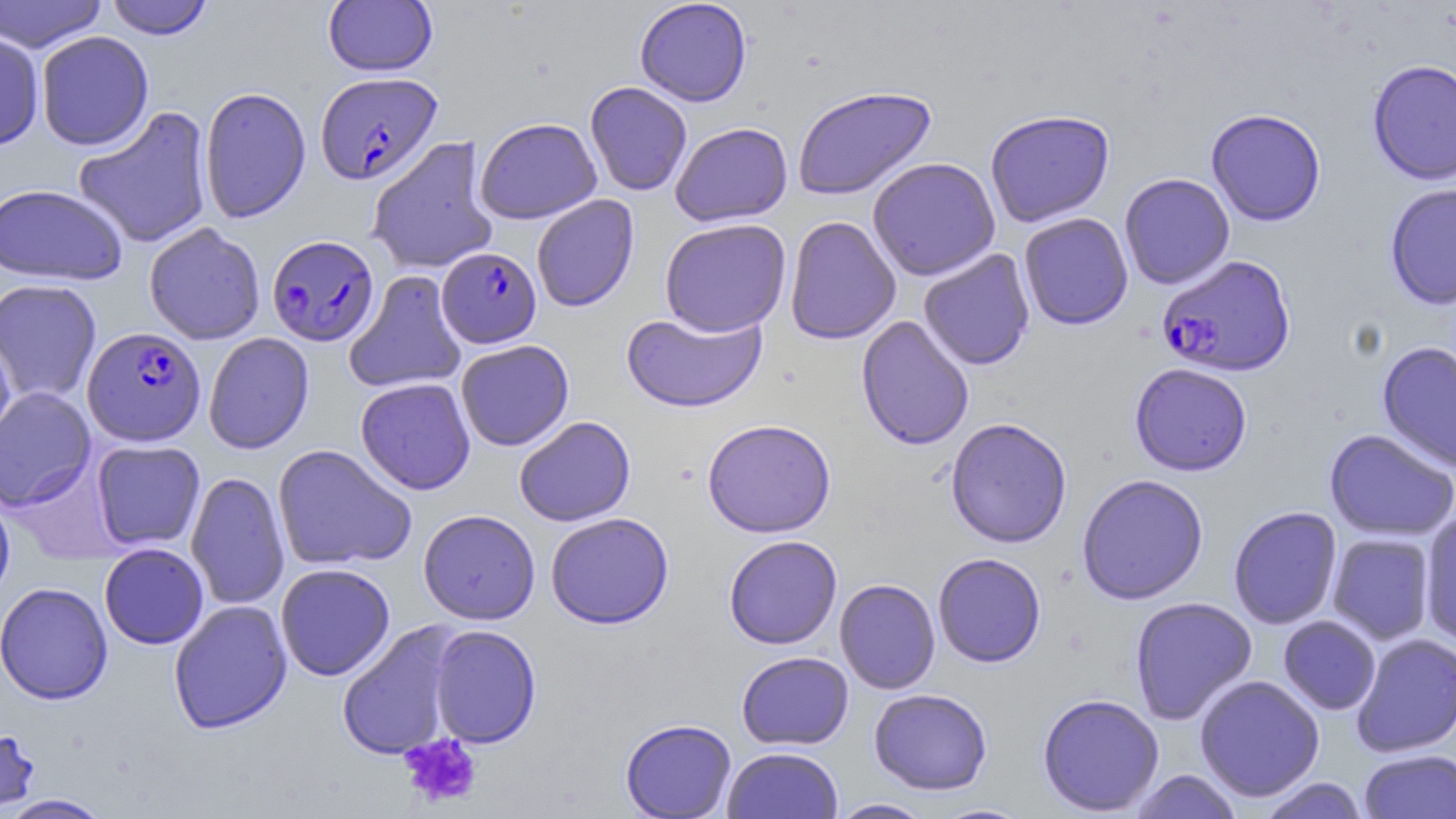

Approximate bounding boxes as (x1, y1, x2, y2) in pixels. Uninfected red blood cell locations: (0, 0, 109, 53), (104, 0, 215, 40), (634, 0, 752, 107), (323, 1, 438, 76), (0, 29, 45, 152), (35, 31, 154, 150), (1367, 59, 1456, 186), (585, 81, 693, 196), (792, 85, 937, 200), (199, 86, 311, 224), (73, 106, 214, 249), (1206, 108, 1326, 227), (985, 110, 1115, 227), (474, 117, 602, 224), (670, 121, 793, 227), (367, 136, 499, 274), (867, 157, 1001, 281), (1119, 173, 1235, 289), (0, 183, 128, 285), (1384, 184, 1456, 310), (531, 195, 640, 312), (1019, 212, 1133, 331), (784, 216, 901, 345), (659, 218, 792, 336), (144, 223, 266, 345), (918, 249, 1035, 370), (344, 270, 468, 394), (0, 279, 102, 405), (621, 310, 767, 413), (856, 316, 974, 451), (0, 331, 17, 461), (203, 333, 314, 455), (455, 339, 574, 451), (1376, 341, 1456, 474), (1129, 363, 1252, 476), (355, 377, 476, 495), (0, 387, 96, 512), (514, 416, 636, 527), (945, 417, 1072, 548), (702, 419, 836, 538), (1323, 429, 1456, 541), (91, 440, 206, 550), (273, 444, 416, 572), (186, 472, 290, 610), (1076, 474, 1209, 605), (0, 486, 16, 610), (1228, 505, 1342, 630), (418, 509, 540, 624), (1419, 510, 1456, 648), (545, 512, 674, 629), (1327, 533, 1436, 644), (723, 535, 843, 649), (99, 544, 209, 650), (932, 553, 1046, 668), (275, 563, 395, 681), (835, 578, 940, 695), (0, 582, 113, 704), (1130, 596, 1257, 725), (168, 600, 292, 734), (1278, 616, 1382, 715), (336, 624, 461, 761), (428, 625, 542, 748), (1352, 633, 1456, 758), (736, 651, 854, 750), (1194, 675, 1325, 801), (868, 688, 993, 795), (1037, 693, 1164, 816), (620, 718, 737, 818), (0, 724, 41, 813), (722, 746, 844, 819), (1358, 749, 1456, 819), (1129, 769, 1243, 819), (1259, 777, 1369, 819), (0, 794, 114, 818), (828, 798, 935, 818), (927, 801, 1034, 818). Plasmodium falciparum-infected red blood cell locations: (315, 71, 443, 184), (267, 234, 380, 346), (436, 247, 541, 349), (1156, 255, 1297, 378), (82, 326, 206, 446). Platelet locations: (399, 733, 483, 808). Slide-level diagnosis: Plasmodium falciparum. Captured at 1000x magnification. One field of a larger specimen. May-Grünwald-Giemsa-stained preparation. Thin blood film. Image is 1456×819 pixels. Light microscopy.